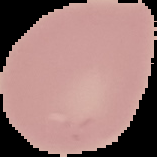

Malaria status: uninfected. From a thin blood smear. Segmented cell region on a black background. Image is 157×157 pixels.